Report the malaria status of this cell.
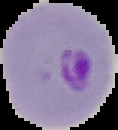

It is parasitized.

image_size: 118×130 pixels
image_type: segmented cell region on a black background
preparation: thin blood film